Locate every malaria parasite and every leukocyte.
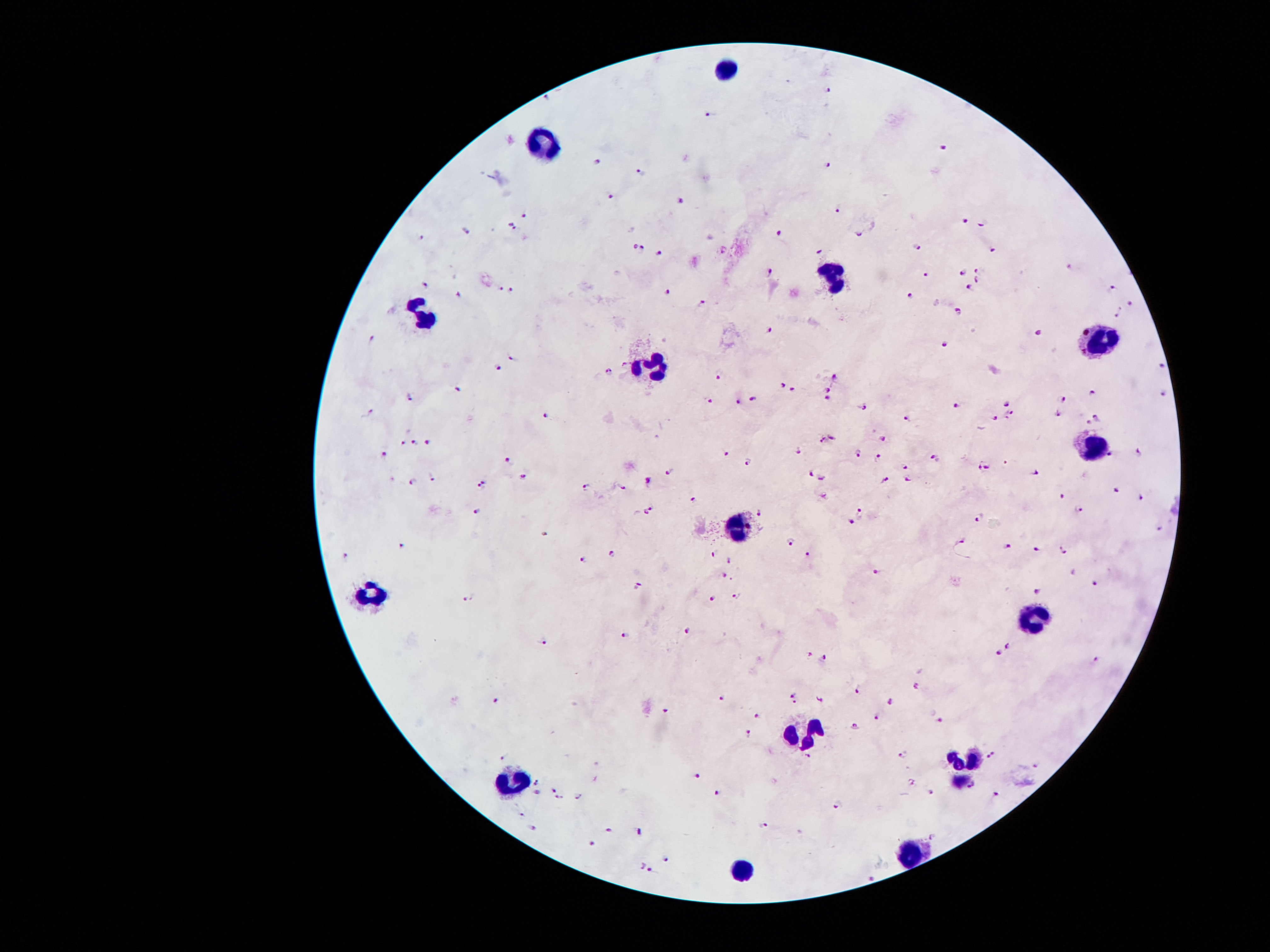

Approximate centers as [x, y] in pixels.
Malaria parasites: [825, 87], [550, 93], [708, 114], [944, 145], [596, 160], [824, 166], [640, 169], [611, 194], [681, 201], [838, 209], [527, 213], [965, 220], [508, 221], [982, 221], [464, 228], [515, 228], [780, 231], [862, 231], [421, 239], [634, 245], [916, 248], [724, 250], [659, 251], [819, 251], [994, 251], [645, 253], [1071, 266], [767, 270], [962, 270], [978, 270], [925, 274], [979, 280], [424, 283], [512, 286], [970, 286], [502, 288], [1111, 289], [665, 294], [911, 296], [455, 297], [702, 304], [1130, 304], [959, 310], [1117, 313], [768, 329], [1036, 332], [372, 339], [946, 343], [513, 356], [1162, 361], [624, 364], [499, 366], [608, 370], [835, 373], [718, 377], [780, 385], [829, 388], [459, 389], [792, 389], [1093, 389], [408, 394], [1160, 394], [751, 397], [825, 397], [1063, 399], [708, 402], [738, 402], [957, 404], [1008, 404], [865, 405], [372, 411], [1011, 411], [546, 415], [905, 415], [1057, 415], [1006, 416], [1098, 416], [994, 418], [1089, 421], [832, 435], [884, 435], [426, 440], [822, 440], [415, 442], [404, 443], [856, 449], [1141, 450], [727, 451], [797, 451], [385, 453], [878, 454], [1111, 454], [935, 456], [746, 459], [508, 461], [905, 465], [989, 465], [669, 467], [978, 467], [808, 470], [1035, 472], [524, 473], [822, 473], [431, 478], [906, 478], [648, 480], [883, 480], [412, 481], [480, 484], [583, 484], [623, 488], [1117, 491], [691, 495], [822, 495], [1062, 495], [1143, 495], [649, 507], [1079, 508], [477, 510], [859, 510], [759, 511], [645, 513], [978, 514], [848, 521], [1160, 529], [542, 530], [402, 541], [789, 541], [962, 541], [1009, 545], [1036, 549], [1062, 549], [806, 551], [613, 554], [345, 556], [713, 556], [583, 559], [730, 560], [878, 573], [724, 575], [1095, 584], [638, 586], [1036, 591], [737, 595], [467, 598], [711, 598], [688, 630], [626, 635], [542, 640], [1005, 644], [998, 651], [808, 654], [824, 655], [1097, 659], [914, 687], [856, 690], [792, 695], [721, 698], [821, 700], [496, 701], [795, 701], [890, 701], [665, 709], [757, 714], [876, 717], [941, 720], [854, 725], [746, 730], [903, 752], [500, 754], [990, 754], [1036, 765], [696, 778], [537, 781], [971, 784], [553, 789], [933, 790], [537, 792], [719, 792], [995, 793], [558, 797], [580, 798], [837, 803], [523, 814], [765, 825], [534, 828], [610, 828], [638, 831], [932, 835], [592, 841], [664, 857], [650, 869], [873, 874].
Leukocytes: [724, 69], [545, 142], [833, 279], [426, 310], [1099, 335], [650, 370], [1092, 447], [735, 524], [374, 591], [1032, 612], [808, 734], [966, 759], [507, 783], [913, 846], [741, 867].

Smartphone photograph taken through the microscope eyepiece. Giemsa-stained preparation. One field from this slide. Patient malaria status: positive for Plasmodium falciparum. Image is 1270×952 pixels. 100x magnification. Thick peripheral-blood smear.